Name the cell type shown.
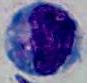

A leukocyte.

Micrograph. 1000x magnification.